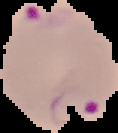

image type = segmented cell region on a black background
result = malaria parasites detected
image size = 118×133 pixels
preparation = thin blood film